Name the blood parasite species.
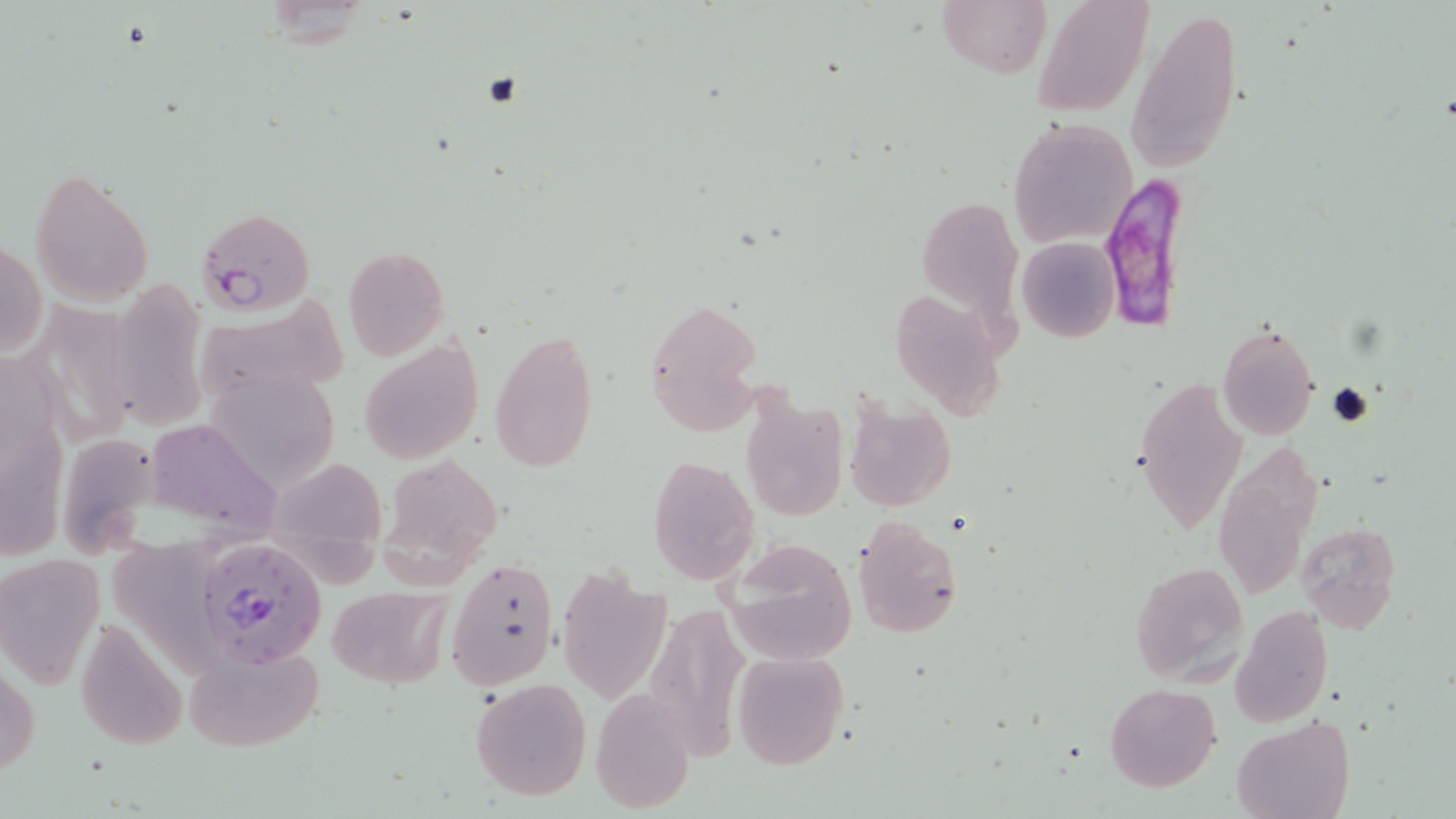
Plasmodium falciparum.

Approximate bounding boxes as (x1, y1, x2, y2) in pixels. Plasmodium falciparum-infected red blood cell locations: (1094, 178, 1186, 327), (195, 207, 316, 316), (201, 539, 325, 667). Uninfected red blood cell locations: (937, 0, 1050, 79), (1031, 0, 1155, 118), (1128, 5, 1242, 177), (1009, 117, 1136, 248), (30, 167, 154, 307), (918, 190, 1023, 345), (1017, 236, 1120, 342), (1, 240, 46, 357), (343, 247, 449, 360), (129, 281, 228, 428), (886, 285, 1010, 422), (190, 297, 350, 407), (644, 300, 762, 435), (39, 305, 143, 462), (1217, 324, 1320, 440), (488, 328, 599, 475), (359, 335, 483, 466), (210, 375, 343, 491), (1134, 376, 1248, 535), (737, 391, 849, 522), (843, 399, 956, 511), (150, 425, 300, 535), (64, 442, 168, 563), (1213, 442, 1324, 608), (382, 454, 506, 574), (648, 455, 759, 584), (272, 466, 390, 594), (851, 516, 963, 640), (110, 517, 208, 677), (1296, 522, 1401, 633), (722, 539, 856, 664), (0, 552, 105, 688), (447, 557, 560, 689), (1130, 561, 1251, 686), (556, 567, 669, 705), (326, 585, 450, 689), (644, 600, 750, 759), (1233, 605, 1333, 727), (74, 619, 187, 751), (184, 641, 325, 752), (729, 651, 850, 769), (1, 660, 38, 781), (469, 677, 592, 802), (1105, 683, 1220, 792), (589, 690, 695, 812), (1233, 715, 1352, 819). 1000x magnification. Optical microscopy. Image is 1456×819 pixels. May-Grünwald-Giemsa stain. Thin blood smear. Single field of view.